Name the parasite shown.
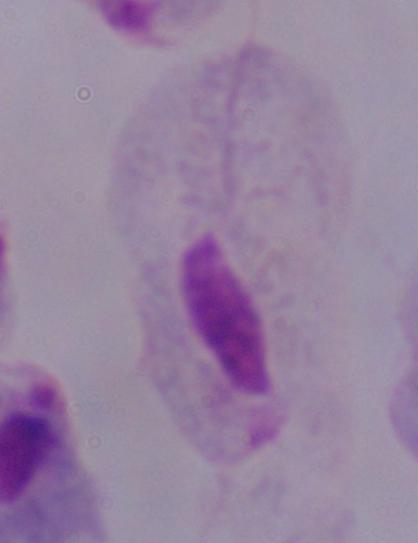

A trichomonad.

{
  "modality": "micrograph",
  "magnification": "1000x"
}